Report the malaria status of this cell.
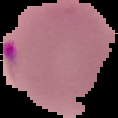

It is parasitized.

preparation = thin blood film
image size = 118×118 pixels
image type = segmented cell region with the area outside set to black